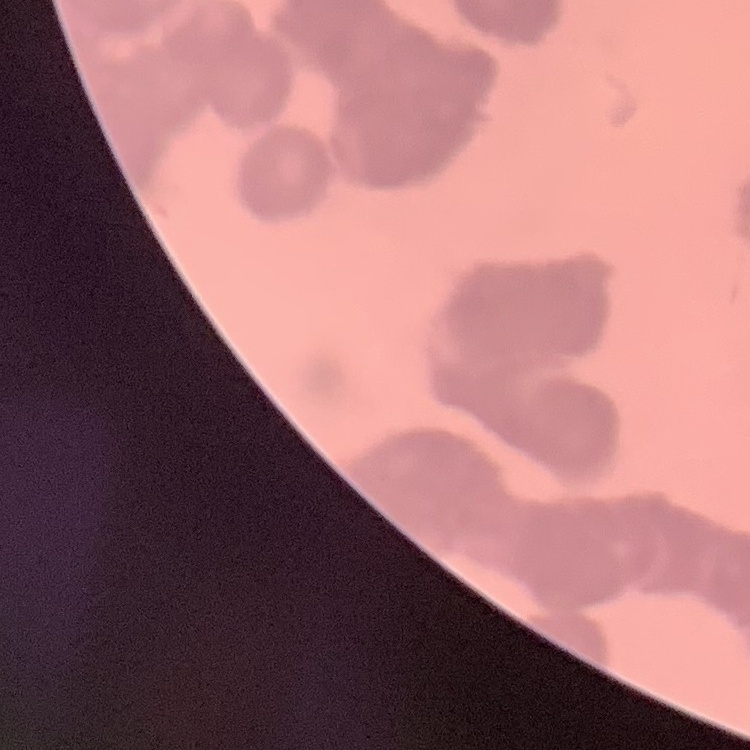
The red blood cells show rouleaux formation. Stained with either Field's or Giemsa. Thin peripheral smear. Square crop of a larger photomicrograph.